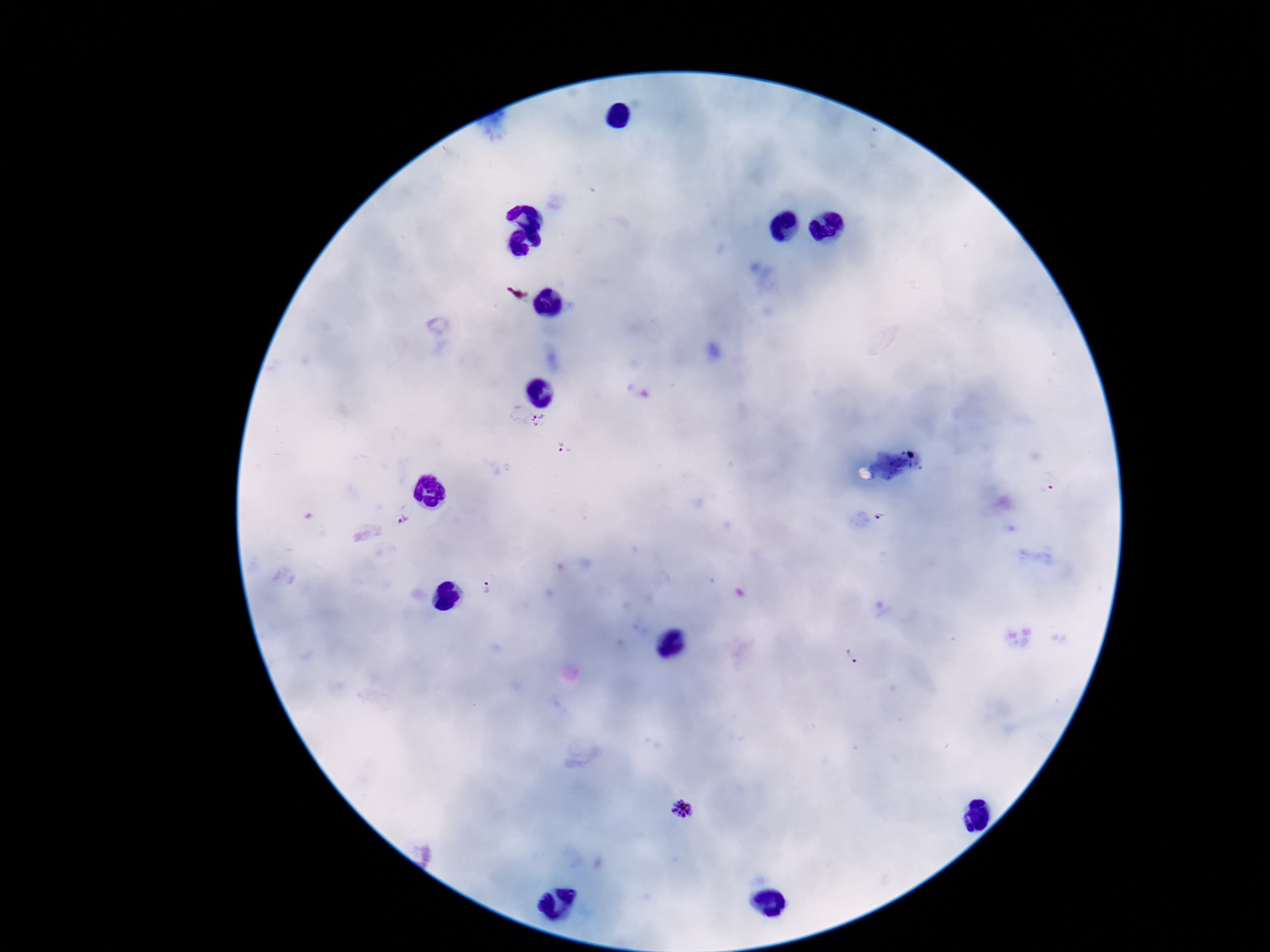

patient malaria status = positive
magnification = 100x
capture = smartphone camera through the microscope eyepiece
field of view = one from this slide
stain = Giemsa
Plasmodium parasite locations = approximate centers as [x, y] in pixels: [540, 419], [563, 447], [884, 517], [411, 521], [486, 588], [681, 808]
image size = 1270×952 pixels
preparation = thick blood film